Locate every leukocyte (white blood cell).
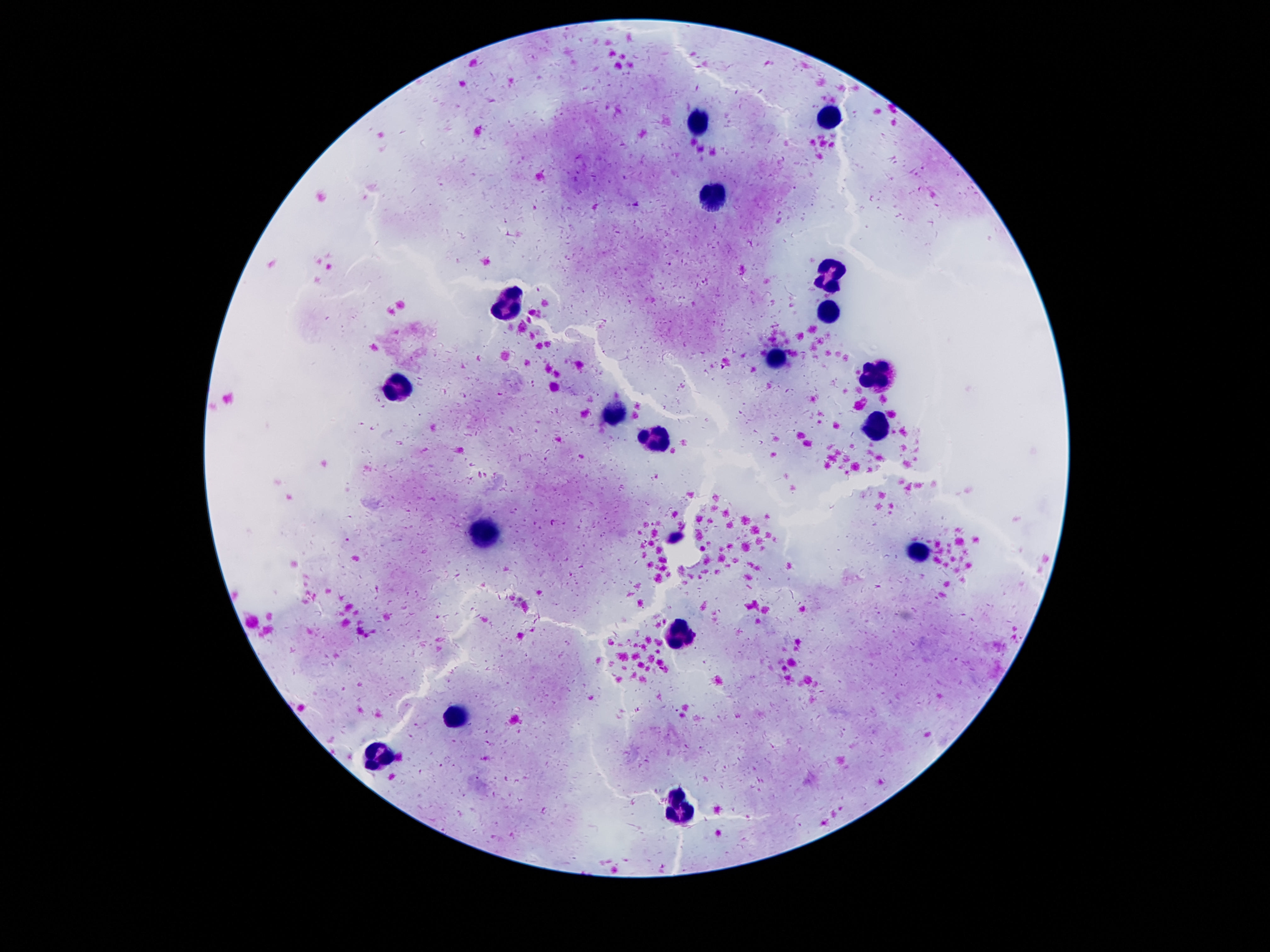

Approximate object centers, in pixels from the top-left corner.
Leukocytes: (x=831, y=116), (x=703, y=122), (x=713, y=196), (x=831, y=275), (x=510, y=301), (x=829, y=316), (x=778, y=359), (x=875, y=374), (x=398, y=389), (x=612, y=416), (x=875, y=424), (x=657, y=439), (x=482, y=531), (x=915, y=553), (x=681, y=635), (x=450, y=714), (x=377, y=758), (x=683, y=815).

image size = 1270×952 pixels
stain = Giemsa
capture = smartphone camera through the microscope eyepiece
preparation = thick blood film
magnification = 100x
field of view = single
patient malaria status = negative